Report the malaria status.
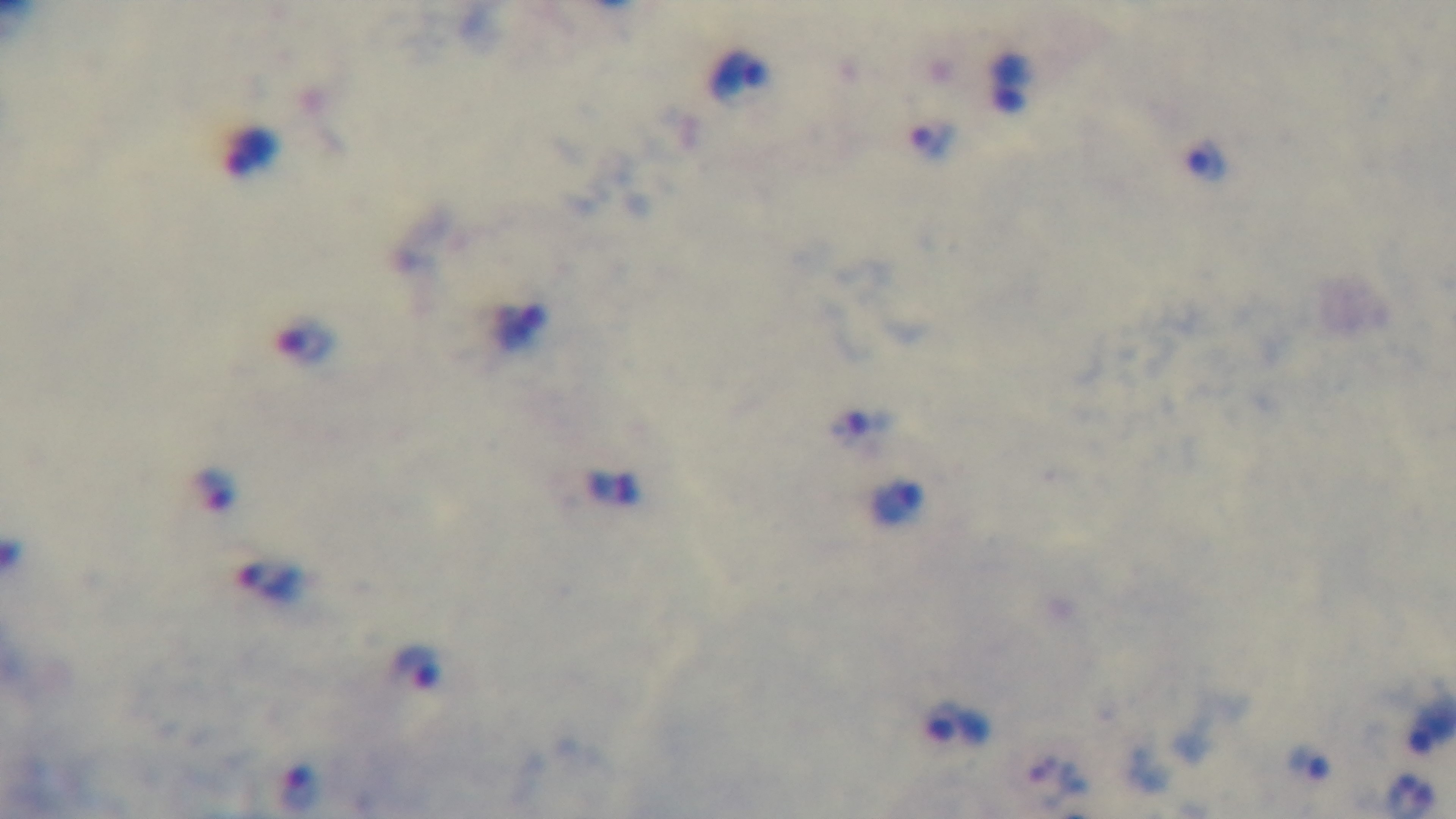

It is infected.

Single field of view. Giemsa-stained. 100x oil-immersion objective. Preparation: thick. Photomicrograph. Mounted 4K digital camera.